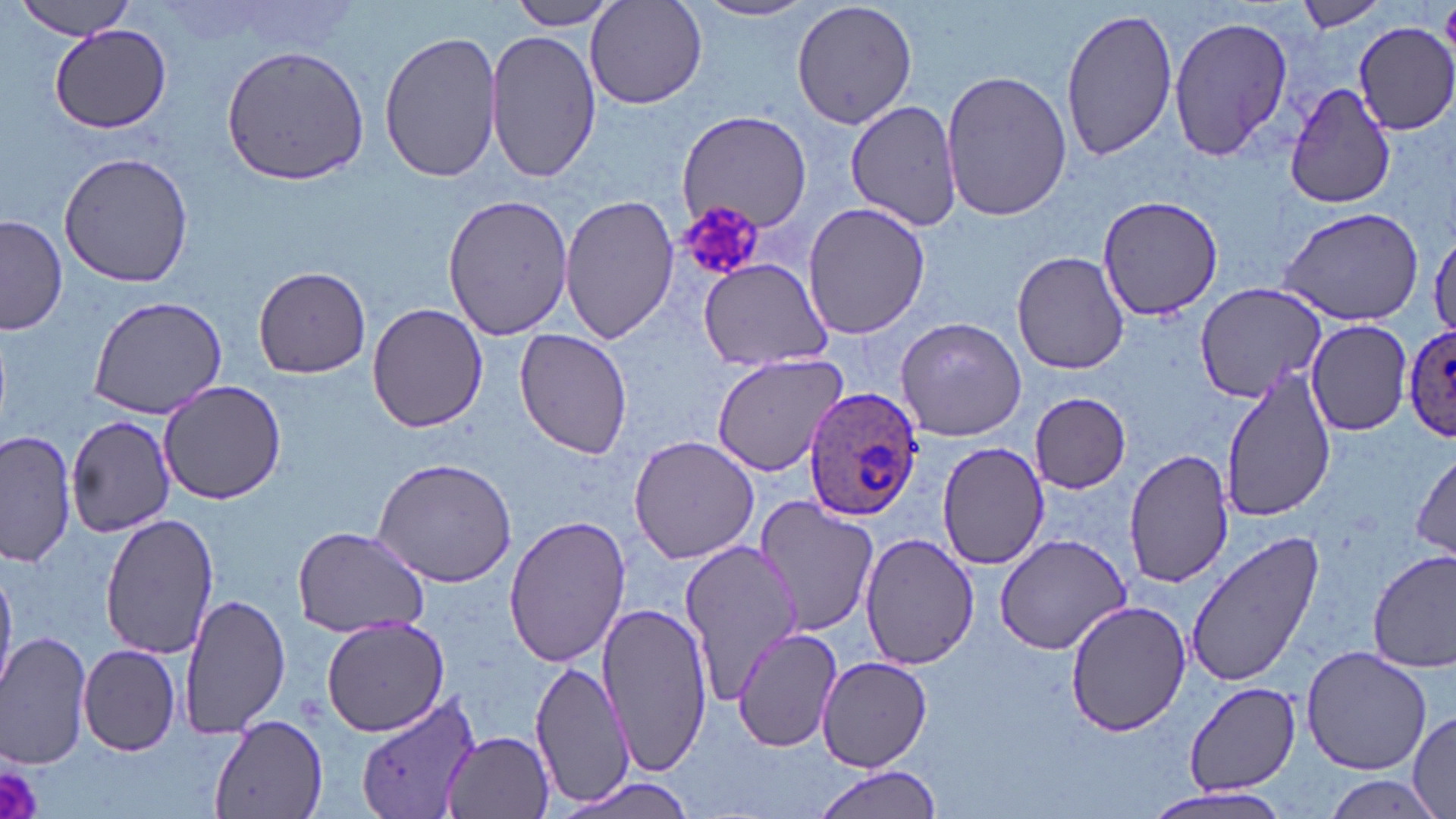
Summary:
  - Coordinate format: approximate bounding boxes as [x1, y1, x2, y2] in pixels
  - Uninfected red blood cell locations: [503, 0, 620, 31], [791, 0, 918, 131], [1292, 0, 1390, 32], [586, 1, 707, 111], [692, 1, 820, 23], [10, 2, 138, 40], [1059, 5, 1179, 164], [1166, 13, 1294, 165], [1350, 21, 1456, 133], [49, 23, 174, 132], [485, 28, 600, 184], [379, 29, 504, 185], [222, 44, 372, 184], [940, 68, 1072, 224], [1284, 81, 1397, 208], [844, 97, 964, 233], [673, 110, 817, 233], [58, 150, 194, 288], [559, 193, 681, 346], [1095, 194, 1223, 320], [442, 195, 574, 342], [803, 202, 928, 340], [1277, 207, 1427, 324], [2, 214, 67, 336], [1430, 228, 1456, 342], [1011, 250, 1131, 375], [698, 257, 836, 370], [253, 265, 372, 379], [1194, 282, 1328, 401], [87, 295, 229, 419], [366, 303, 488, 433], [896, 318, 1026, 441], [1306, 319, 1413, 436], [514, 330, 632, 460], [710, 352, 849, 478], [1219, 373, 1337, 523], [157, 381, 288, 505], [1028, 393, 1131, 493], [64, 413, 178, 535], [2, 428, 77, 569], [628, 435, 760, 564], [936, 441, 1049, 571], [1410, 448, 1456, 565], [1125, 449, 1235, 589], [373, 457, 519, 588], [753, 496, 880, 636], [98, 513, 221, 660], [503, 516, 631, 669], [290, 525, 431, 638], [1186, 530, 1322, 689], [857, 532, 980, 670], [993, 532, 1133, 656], [674, 539, 805, 701], [1369, 550, 1456, 674], [0, 560, 17, 700], [178, 593, 290, 740], [1064, 598, 1194, 737], [597, 602, 714, 778], [321, 617, 451, 736], [732, 625, 842, 752], [0, 632, 93, 768], [78, 645, 182, 754], [1301, 647, 1432, 775], [816, 655, 934, 771], [531, 659, 633, 808], [1183, 682, 1304, 795], [356, 693, 479, 818], [1410, 710, 1455, 817], [211, 719, 329, 819], [441, 731, 556, 818], [810, 764, 947, 819], [558, 773, 701, 817], [1318, 776, 1449, 818], [1139, 785, 1297, 819]
  - Platelet locations: [678, 198, 765, 283], [0, 759, 44, 819]
  - Plasmodium ovale-infected red blood cell locations: [1403, 325, 1454, 441], [803, 389, 922, 521]
  - Slide-level diagnosis: Plasmodium ovale
  - Modality: optical microscopy
  - Magnification: 1000x
  - Preparation: thin blood film
  - Stain: May-Grünwald-Giemsa
  - Image size: 1456×819 pixels
  - Field of view: single